Give the position of every Plasmodium parasite visible.
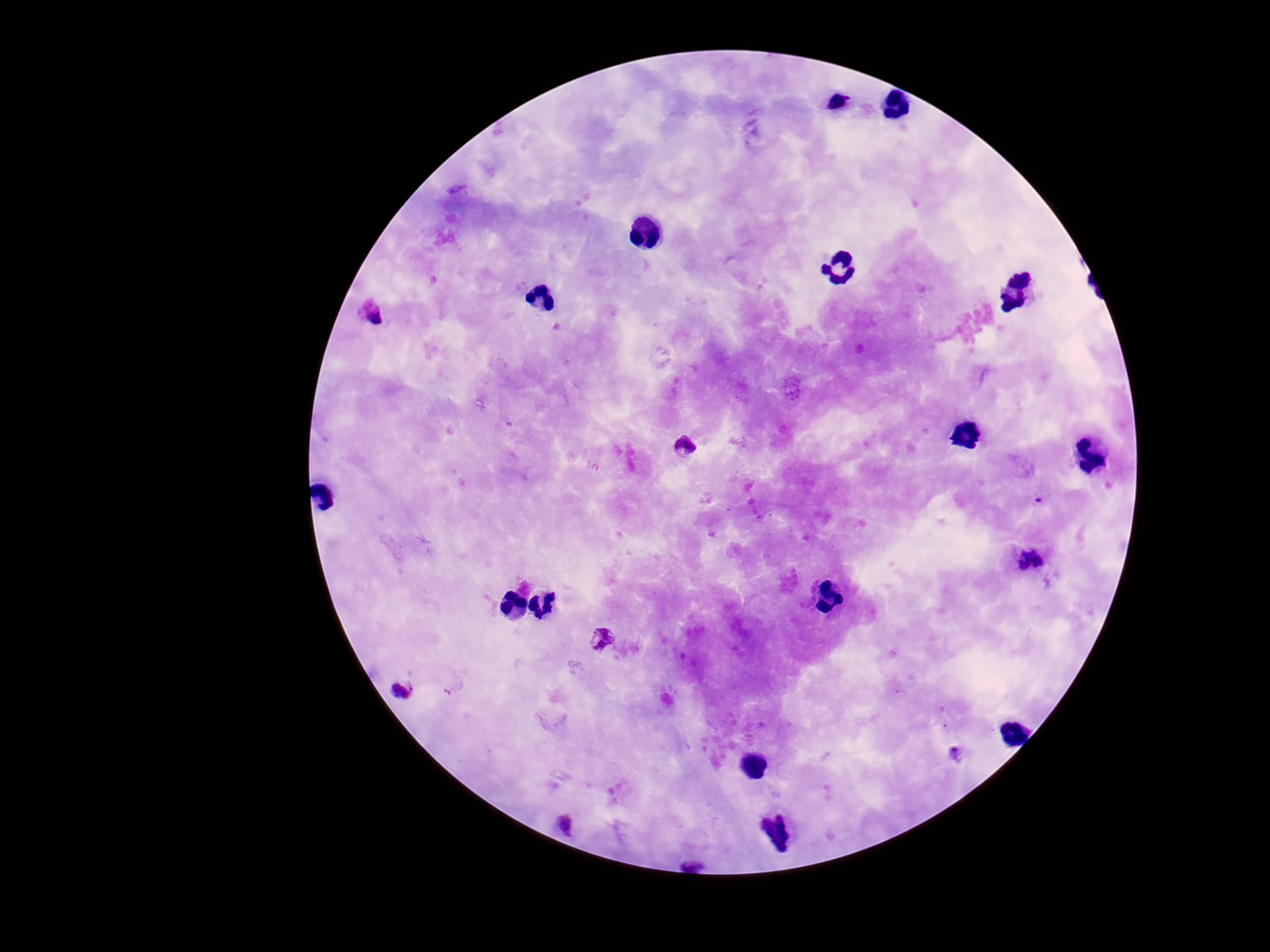

Approximate centers as {x, y} in pixels.
Plasmodium parasites: {837, 102}, {373, 312}, {685, 446}, {1031, 558}, {601, 639}, {403, 690}, {563, 825}.

100x magnification. Patient malaria status: positive. One field from this slide. Image is 1270×952 pixels. Smartphone photograph taken through the microscope eyepiece. Giemsa-stained preparation. Thick blood smear.